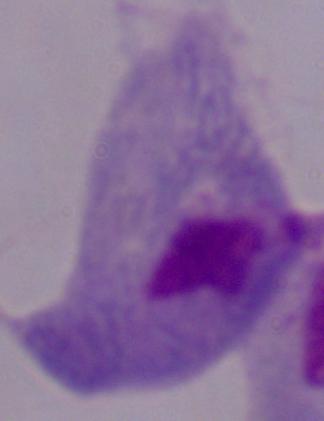

identification: trichomonad
magnification: 1000x
modality: micrograph